Report the malaria status of this cell.
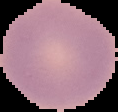

It is uninfected.

From a thin blood smear. Segmented cell region on a black background. Image is 118×112 pixels.